Identify the preparation type.
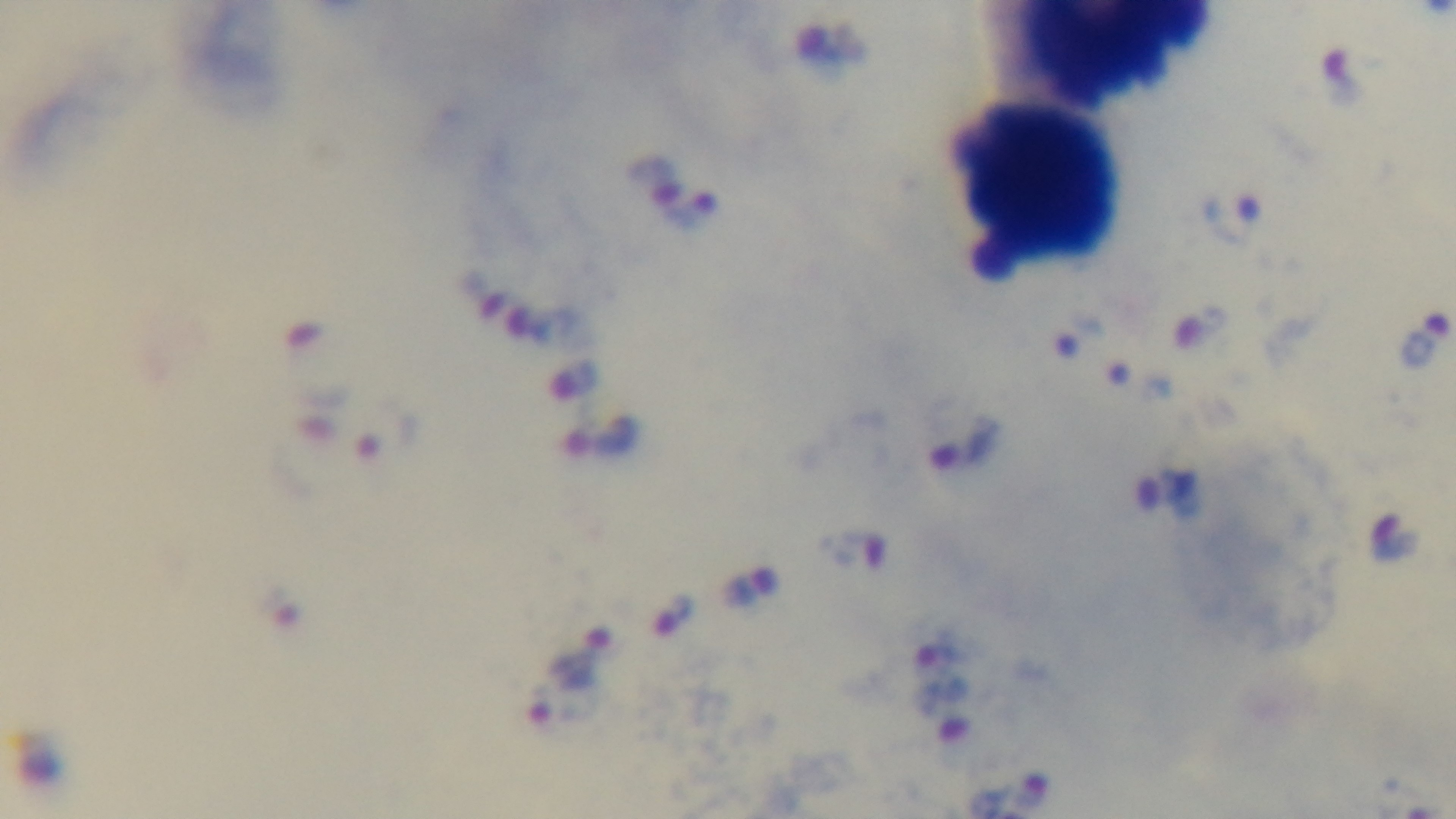

It is a thick blood film.

Oil-immersion objective, 100x. Captured with a mounted 4K digital camera. One field from the slide. Photomicrograph. Malaria status: positive. Giemsa stain.